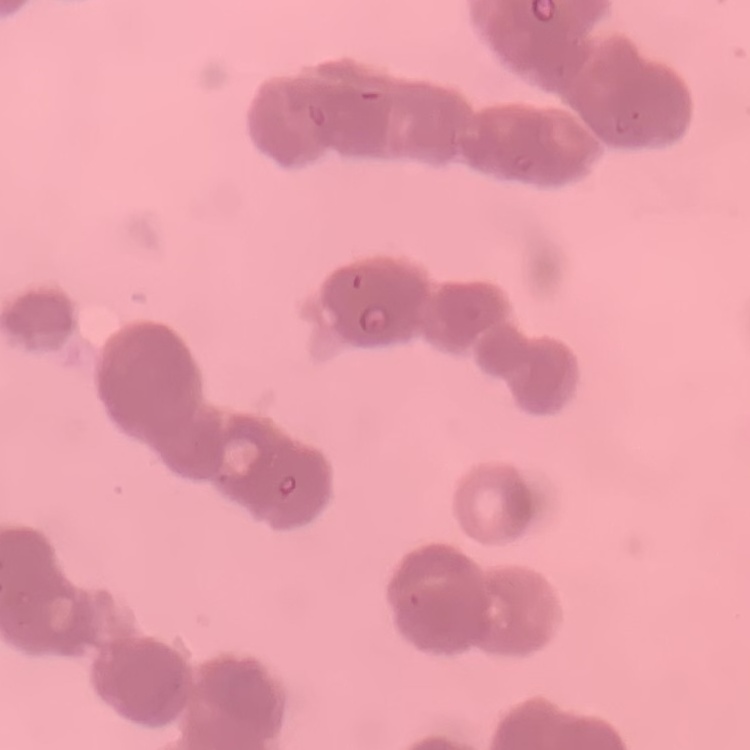

red blood cell morphology = rouleaux formation
preparation = thin blood film
stain = Field's or Giemsa
image type = one tile cut from a larger photomicrograph